Name the cell type shown.
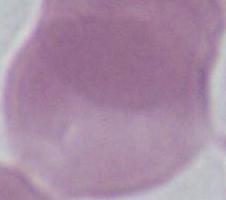
This is an erythrocyte.

Summary:
  - Magnification: 1000x
  - Modality: micrograph